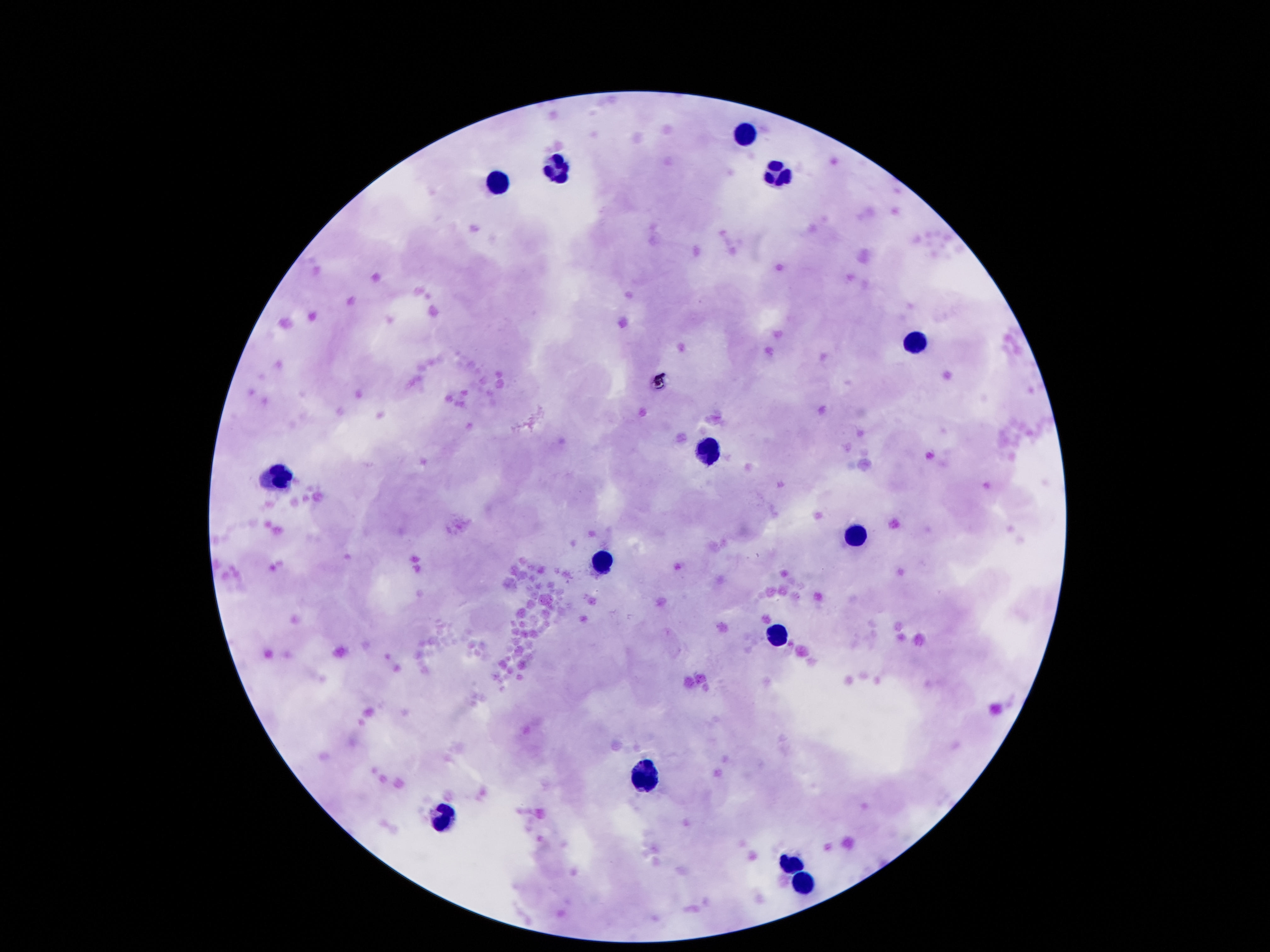
Approximate centers as (x, y) in pixels. Leukocyte locations: (748, 135), (558, 164), (778, 178), (501, 181), (910, 343), (704, 451), (282, 470), (853, 538), (604, 560), (780, 635), (648, 779), (442, 820), (786, 858), (805, 885). Giemsa-stained preparation. Image is 1270×952 pixels. Patient malaria status: negative. Single field of view. Photographed through the microscope eyepiece with a smartphone camera. 100x magnification. Thick blood smear.